Give the extent of all Plasmodium vivax-infected red blood cells.
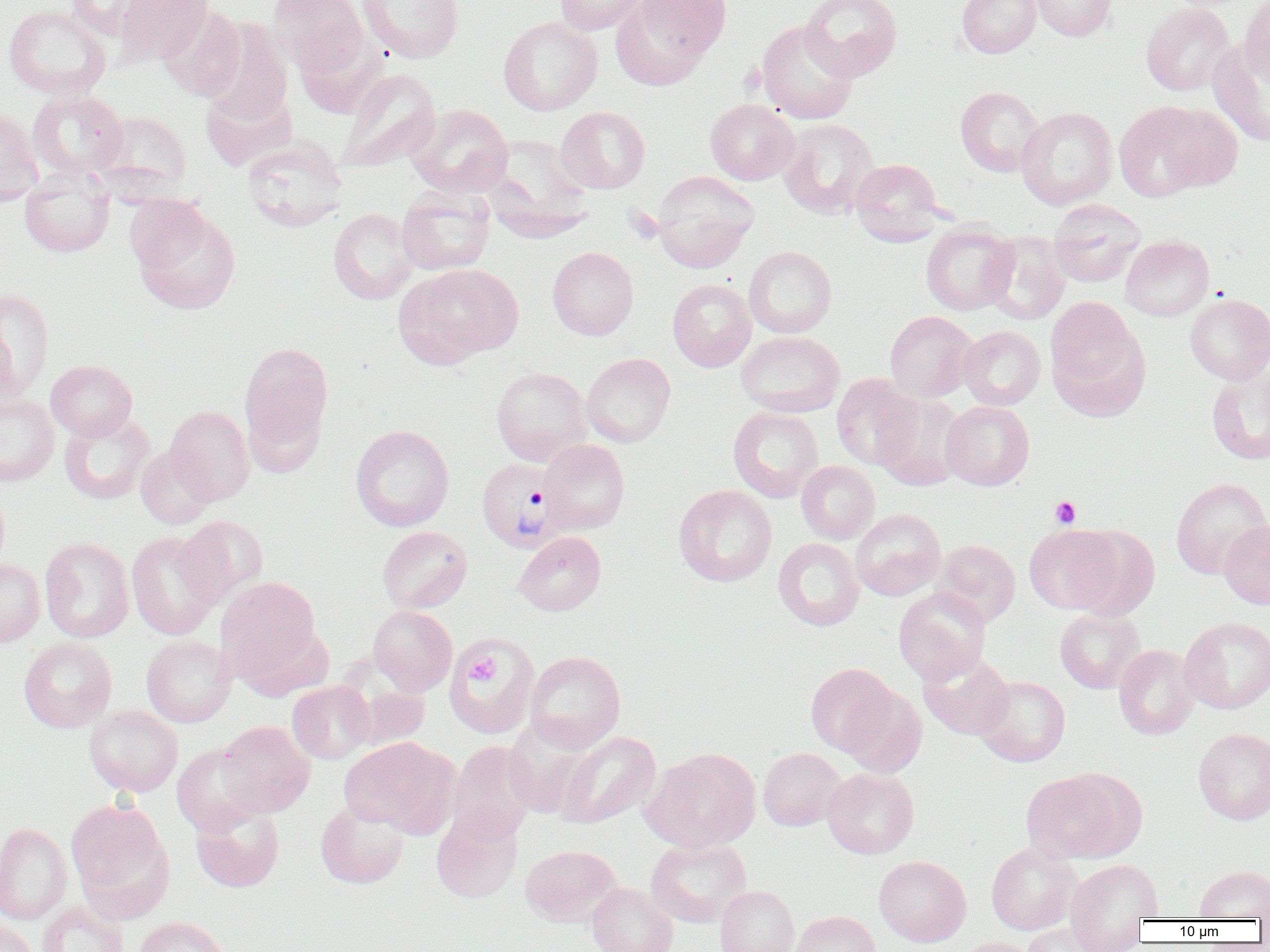

Approximate bounding boxes as (x1, y1, x2, y2) in pixels.
Plasmodium vivax-infected red blood cells: (476, 457, 568, 553).

Uninfected red blood cell locations: (65, 0, 160, 39), (113, 0, 213, 66), (267, 0, 367, 75), (554, 0, 648, 35), (610, 0, 716, 89), (800, 0, 903, 81), (956, 0, 1041, 58), (1031, 0, 1116, 41), (1240, 0, 1270, 87), (358, 1, 463, 63), (1140, 3, 1235, 95), (3, 4, 111, 99), (158, 5, 247, 101), (498, 16, 602, 115), (756, 20, 859, 124), (201, 21, 294, 126), (1208, 40, 1270, 147), (337, 69, 441, 173), (955, 86, 1044, 176), (28, 90, 129, 180), (705, 99, 799, 185), (1114, 101, 1222, 201), (406, 103, 513, 197), (556, 106, 650, 194), (1016, 107, 1117, 210), (0, 108, 43, 206), (94, 110, 191, 194), (778, 118, 880, 219), (242, 138, 347, 232), (850, 158, 945, 245), (19, 170, 114, 257), (652, 171, 759, 273), (397, 188, 495, 276), (128, 200, 240, 314), (1048, 200, 1146, 287), (328, 208, 419, 304), (920, 222, 1019, 316), (984, 231, 1071, 325), (1120, 235, 1215, 321), (743, 246, 837, 338), (547, 247, 639, 340), (395, 264, 522, 367), (667, 278, 756, 372), (0, 289, 54, 398), (1185, 293, 1270, 384), (1045, 297, 1149, 417), (884, 311, 978, 402), (958, 326, 1045, 410), (736, 331, 845, 417), (239, 341, 333, 460), (581, 353, 676, 447), (46, 360, 137, 441), (491, 367, 591, 465), (1206, 368, 1270, 465), (831, 374, 921, 470), (0, 393, 59, 487), (874, 393, 968, 491), (940, 401, 1034, 490), (165, 405, 255, 504), (727, 407, 823, 503), (59, 412, 155, 504), (351, 425, 454, 531), (538, 439, 630, 535), (135, 445, 217, 529), (796, 461, 879, 544), (1171, 477, 1269, 580), (0, 484, 10, 577), (674, 484, 777, 586), (851, 508, 946, 601), (176, 516, 268, 605), (1218, 520, 1270, 609), (1024, 524, 1122, 614), (1068, 525, 1160, 620), (377, 526, 473, 613), (125, 530, 221, 641), (514, 531, 606, 615), (39, 537, 135, 642), (773, 538, 865, 630), (932, 539, 1020, 626), (0, 558, 45, 647), (215, 576, 321, 683), (893, 587, 991, 684), (368, 605, 457, 695), (1055, 608, 1145, 694), (1180, 617, 1270, 713), (443, 633, 541, 739), (141, 634, 236, 727), (19, 637, 117, 733), (1114, 644, 1199, 740), (525, 650, 626, 751), (918, 651, 1014, 740), (805, 662, 901, 758), (975, 676, 1070, 767), (287, 680, 375, 764), (838, 687, 926, 777), (84, 705, 183, 796), (217, 721, 315, 817), (1193, 728, 1270, 825), (556, 731, 661, 829), (340, 736, 458, 836), (448, 741, 539, 842), (172, 744, 264, 836), (641, 747, 761, 852), (758, 747, 845, 831), (326, 767, 432, 872), (822, 768, 919, 859), (1021, 770, 1138, 864), (66, 799, 174, 919), (190, 801, 285, 893), (316, 801, 409, 889), (430, 808, 523, 903), (0, 823, 72, 924), (645, 838, 750, 927), (986, 841, 1081, 935), (520, 844, 621, 927), (874, 856, 971, 947), (1065, 859, 1162, 949), (1195, 865, 1270, 920), (587, 883, 678, 952), (715, 885, 799, 952), (37, 901, 128, 952), (790, 911, 881, 952), (133, 917, 232, 952), (0, 918, 38, 952), (1022, 922, 1116, 952), (954, 937, 1043, 952). Platelet locations: (1050, 496, 1080, 528), (469, 657, 499, 682). Slide-level diagnosis: Plasmodium vivax. Light microscopy. Captured at 1000x magnification. Thin blood film. Image is 1270×952 pixels. Single field of view.